Locate every malaria parasite and identify its life-cycle stage.
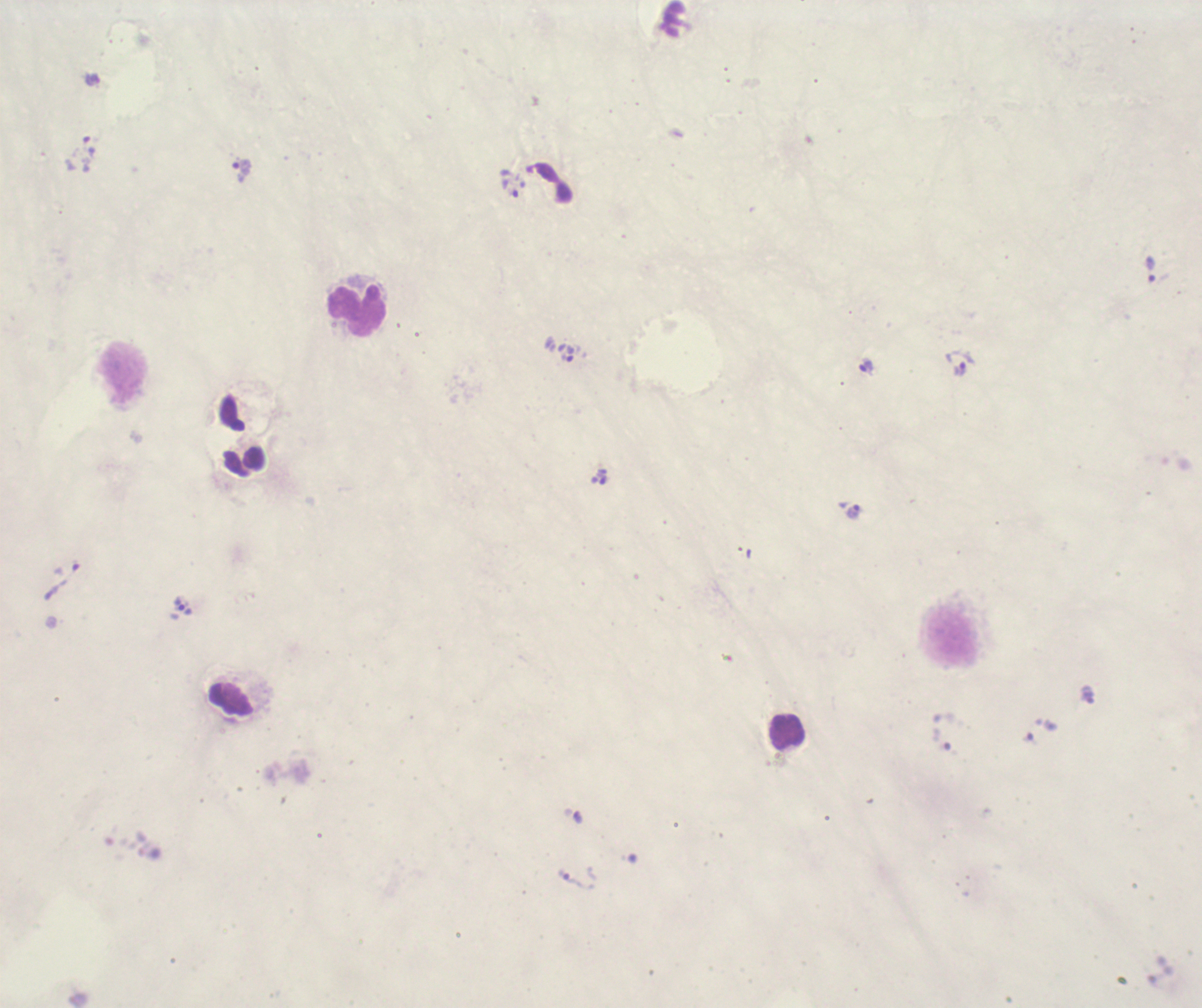
Approximate centers as {x, y} in pixels.
Trophozoites: {242, 171}, {510, 184}, {1150, 270}, {567, 353}, {959, 363}, {867, 367}, {853, 513}, {184, 606}, {571, 881}.
No schizont or gametocyte forms observed.

coordinate format = approximate centers as {x, y} in pixels
leukocyte locations = {356, 311}, {951, 638}, {787, 731}
image size = 1202×1008 pixels
coloration quality = bad
magnification = 100x
preparation = thick blood film
context = previously used in a real diagnosis
field of view = one from this slide
stain = Romanowsky
background quality = unsatisfactory